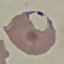
malaria status = parasitized
preparation = thin smear
image type = automatically extracted cell patch, resized to 64 × 64 pixels
capture = smartphone camera at the microscope eyepiece
stain = Giemsa